Look for Plasmodium parasites.
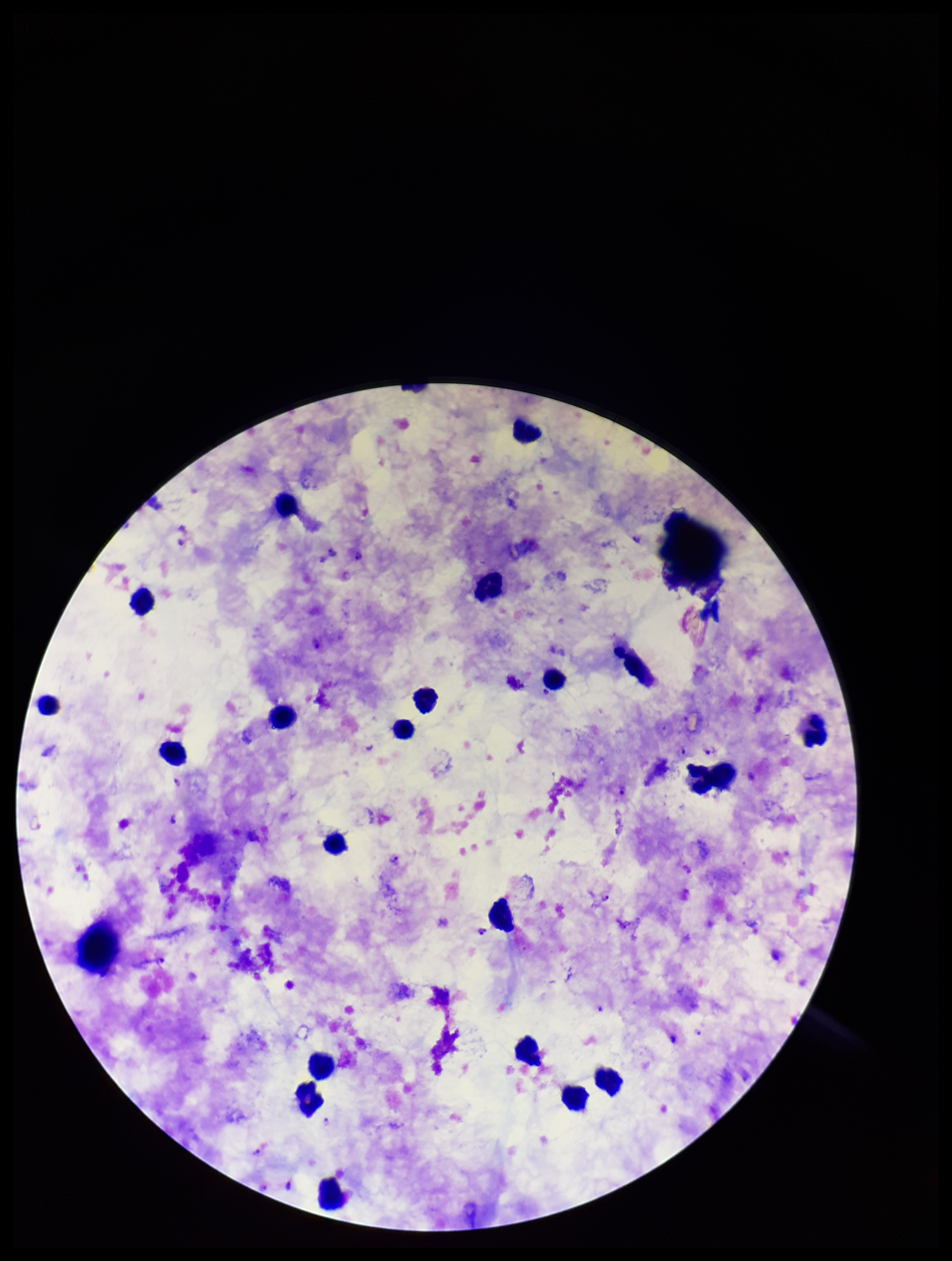

Identified.

{
  "parasite_count": 12,
  "preparation": "thick",
  "capture": "smartphone photograph through the microscope eyepiece",
  "patient_malaria_status": "positive",
  "field_of_view": "single",
  "species_reported_for_this_patient": "Plasmodium falciparum",
  "image_size": "952×1261 pixels",
  "stain": "Giemsa",
  "leukocyte_count": 19
}